State which parasite is depicted.
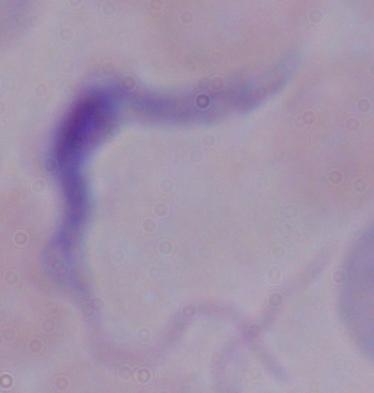
A trypanosome.

modality = photomicrograph
magnification = 1000x